Identify the parasite.
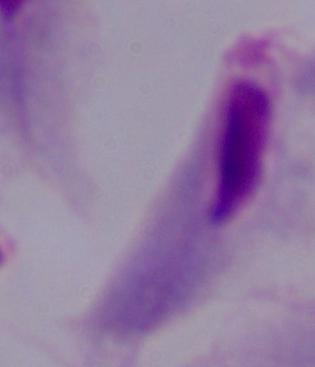
This is a trichomonad.

{
  "modality": "micrograph",
  "magnification": "1000x"
}